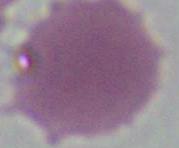

identification = red blood cell
modality = photomicrograph
magnification = 1000x